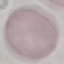
result: negative for malaria parasites
image_type: automatically extracted cell patch, resized to 64 × 64 pixels
capture: smartphone camera at the microscope eyepiece
preparation: thin smear
stain: Giemsa